Find each parasitized red blood cell.
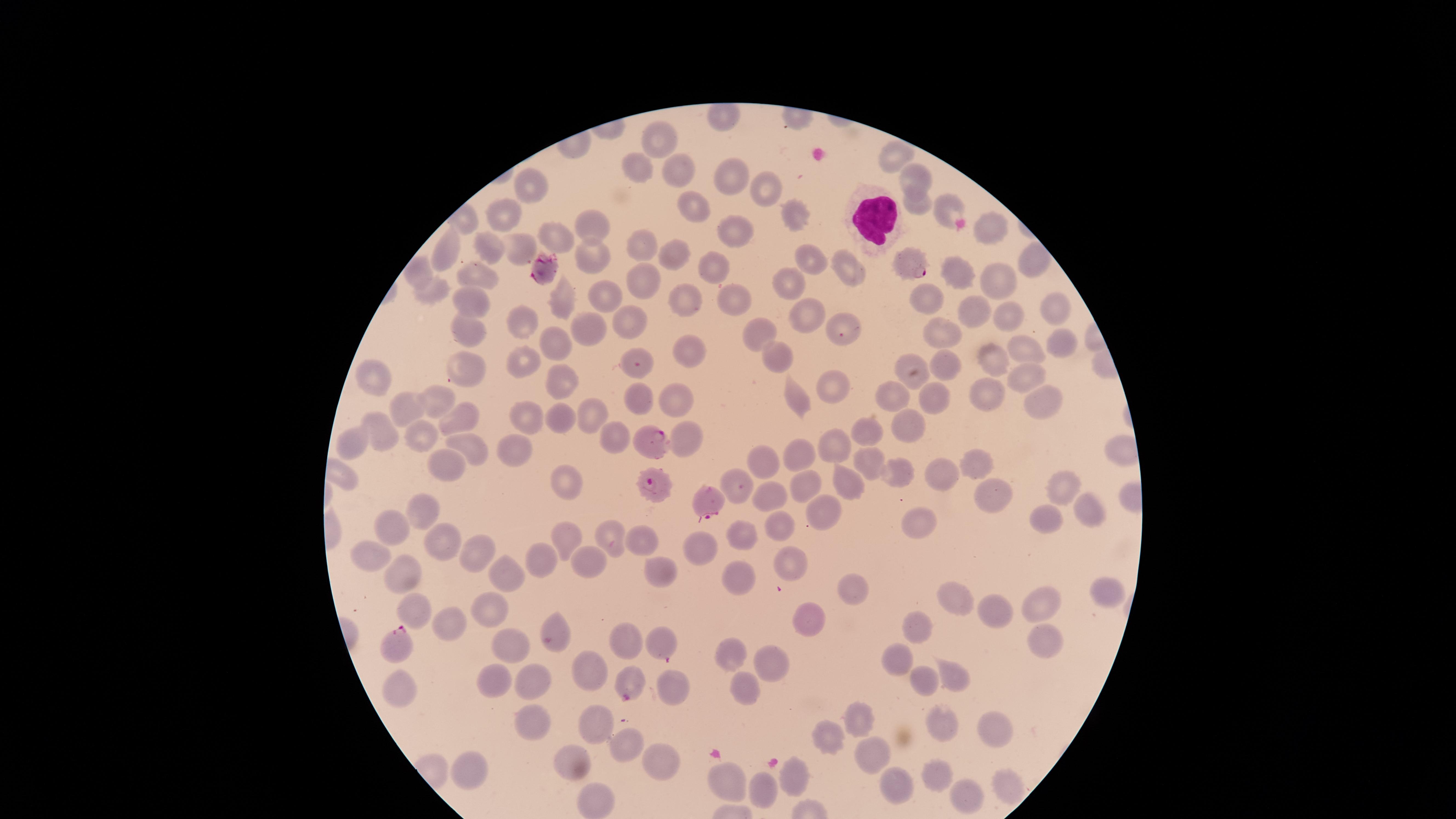

Approximate marker points as (x, y) in pixels.
Parasitized red blood cells: (914, 263), (545, 267), (653, 438), (659, 488), (710, 504), (396, 644), (629, 687).

Approximate marker points as (x, y) in pixels.
Summary:
  - White blood cells: (871, 216)
  - Uninfected red blood cells: (656, 142), (892, 154), (633, 164), (681, 169), (734, 174), (910, 177), (528, 185), (765, 190), (687, 201), (921, 203), (946, 207), (791, 208), (503, 219), (595, 223), (734, 225), (992, 227), (555, 235), (486, 244), (446, 245), (641, 245), (519, 250), (677, 250), (593, 256), (811, 258), (1032, 263), (849, 265), (716, 268), (951, 268), (419, 270), (475, 275), (645, 277), (997, 277), (788, 282), (428, 291), (926, 295), (564, 296), (686, 296), (729, 296), (604, 297), (467, 299), (1054, 307), (969, 309), (807, 311), (1005, 317), (631, 320), (846, 322), (588, 324), (470, 327), (524, 327), (944, 332), (758, 333), (1056, 340), (560, 341), (1019, 345), (687, 348), (777, 355), (996, 357), (909, 359), (944, 360), (526, 361), (468, 363), (642, 366), (1026, 371), (554, 377), (372, 379), (834, 383), (988, 391), (889, 395), (676, 396), (798, 398), (934, 398), (644, 399), (1042, 399), (444, 400), (405, 405), (587, 411), (528, 415), (461, 416), (560, 416), (908, 417), (870, 431), (384, 434), (611, 435), (426, 436), (690, 439), (351, 441), (471, 447), (513, 447), (833, 447), (795, 453), (868, 459), (758, 463), (445, 465), (982, 465), (936, 472), (900, 475), (846, 478), (566, 482), (1061, 483), (731, 484), (808, 487), (986, 490), (768, 493), (422, 508), (1089, 509), (826, 510), (917, 517), (1046, 518), (783, 519), (395, 530), (443, 536), (744, 536), (569, 537), (607, 538), (645, 540), (703, 544), (474, 551), (374, 559), (540, 559), (589, 560), (788, 560), (506, 571), (660, 573), (407, 576), (742, 579), (856, 586), (1099, 590), (950, 595), (1040, 602), (416, 609), (493, 609), (997, 611), (806, 617), (444, 623), (555, 625), (919, 625), (623, 635), (657, 639), (513, 640), (1044, 643), (731, 652), (897, 655), (772, 659), (589, 669), (496, 674), (956, 675), (924, 677), (527, 679), (674, 679), (741, 683), (402, 692), (858, 716), (598, 718), (529, 719), (940, 725), (998, 729), (825, 731), (620, 747), (576, 757), (873, 757), (661, 760), (470, 769), (936, 770), (792, 777), (728, 778), (1003, 783), (767, 788), (900, 791), (962, 796), (589, 800)
  - Image size: 1456×819 pixels
  - Visible region: circular
  - Species: Plasmodium falciparum
  - Preparation: thin blood film
  - Stain: Giemsa
  - Capture: smartphone photograph through the microscope eyepiece
  - Field of view: single